Outline platelets.
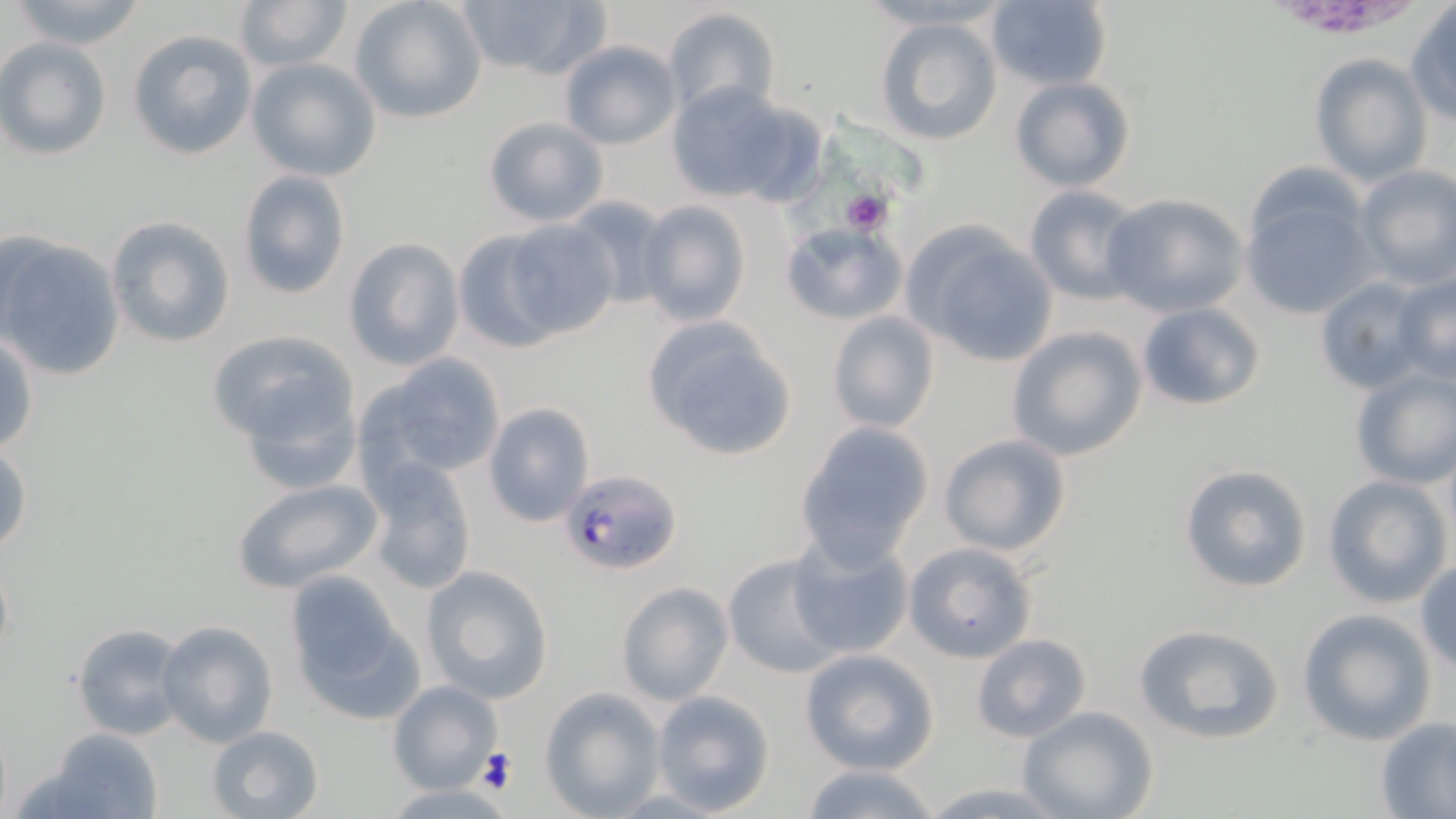

Approximate bounding boxes as (x1, y1, x2, y2) in pixels.
Platelets: (839, 191, 893, 236), (477, 747, 516, 795).

Summary:
  - Uninfected red blood cell locations: (7, 0, 151, 51), (234, 0, 352, 74), (349, 0, 486, 124), (454, 0, 607, 81), (857, 1, 1011, 33), (984, 1, 1112, 91), (1405, 4, 1456, 125), (663, 8, 781, 123), (875, 16, 1003, 147), (127, 29, 257, 159), (0, 39, 111, 160), (558, 41, 681, 150), (1309, 53, 1431, 186), (247, 58, 381, 182), (1010, 77, 1135, 193), (666, 83, 818, 207), (481, 116, 610, 229), (1352, 165, 1456, 288), (236, 169, 352, 300), (1022, 185, 1144, 305), (1242, 189, 1378, 320), (1100, 193, 1249, 317), (560, 197, 676, 314), (634, 200, 753, 325), (104, 215, 235, 349), (498, 216, 620, 341), (778, 219, 907, 326), (903, 223, 1059, 368), (451, 229, 569, 352), (0, 232, 126, 380), (341, 238, 464, 369), (1395, 269, 1456, 386), (1313, 275, 1433, 394), (1135, 302, 1265, 412), (826, 309, 941, 436), (640, 316, 797, 463), (206, 327, 365, 468), (1007, 327, 1146, 461), (1, 330, 37, 458), (358, 353, 510, 484), (1349, 366, 1456, 488), (482, 402, 597, 528), (793, 421, 934, 566), (939, 433, 1072, 557), (0, 443, 31, 558), (360, 458, 480, 597), (1178, 463, 1313, 594), (1322, 475, 1452, 608), (230, 477, 383, 594), (788, 533, 914, 661), (902, 542, 1038, 665), (722, 556, 841, 679), (1415, 559, 1456, 672), (420, 564, 555, 702), (285, 572, 426, 724), (616, 581, 733, 706), (1298, 609, 1435, 745), (154, 620, 279, 749), (70, 622, 190, 742), (1132, 622, 1287, 745), (969, 634, 1092, 742), (798, 649, 939, 774), (387, 679, 500, 794), (540, 688, 664, 817), (650, 689, 774, 815), (1016, 705, 1158, 819), (1375, 716, 1456, 817), (206, 724, 325, 818), (36, 729, 164, 819), (796, 763, 946, 819), (915, 781, 1074, 817)
  - Plasmodium falciparum-infected red blood cell locations: (560, 468, 684, 574)
  - Slide-level diagnosis: Plasmodium falciparum
  - Stain: May-Grünwald-Giemsa
  - Preparation: thin blood smear
  - Magnification: 1000x
  - Modality: optical microscopy
  - Image size: 1456×819 pixels
  - Field of view: single